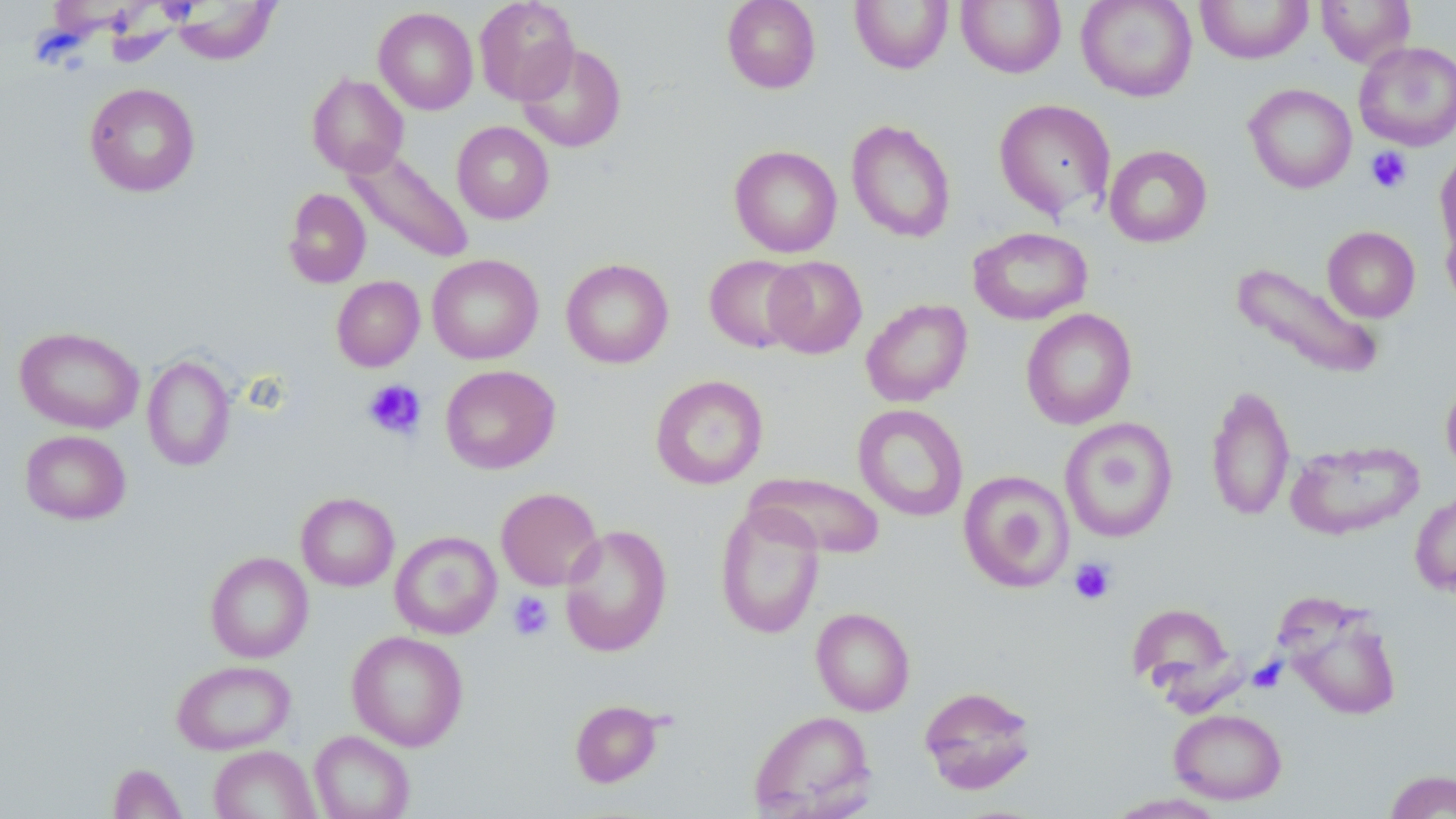

slide_level_diagnosis: no evidence of blood parasites
image_size: 1456×819 pixels
platelet_locations: 'approximate bounding boxes as [x1, y1, x2, y2] in pixels: [1365, 146, 1412, 194], [362, 379, 427, 440], [1069, 558, 1116, 605], [508, 591, 554, 640]'
modality: light microscopy
uninfected_red_blood_cell_locations: 'approximate bounding boxes as [x1, y1, x2, y2] in pixels: [473, 0, 579, 104], [721, 0, 821, 93], [850, 0, 952, 74], [956, 0, 1066, 78], [1076, 0, 1198, 102], [1195, 0, 1313, 64], [1316, 0, 1416, 68], [172, 1, 280, 65], [374, 7, 478, 114], [1353, 41, 1456, 151], [517, 43, 626, 152], [306, 73, 409, 178], [84, 82, 200, 197], [1244, 84, 1357, 193], [993, 98, 1115, 221], [846, 119, 956, 243], [452, 121, 554, 224], [1103, 144, 1213, 248], [729, 145, 843, 258], [1436, 146, 1456, 264], [345, 148, 474, 265], [283, 187, 371, 288], [1440, 208, 1456, 314], [1322, 226, 1420, 322], [968, 227, 1092, 325], [427, 254, 543, 364], [704, 255, 808, 353], [763, 255, 867, 359], [561, 258, 674, 369], [1232, 262, 1385, 380], [331, 276, 425, 372], [861, 298, 973, 407], [1021, 308, 1137, 430], [15, 326, 144, 434], [142, 355, 235, 471], [440, 365, 561, 474], [1440, 373, 1456, 478], [650, 374, 767, 489], [1205, 384, 1295, 522], [853, 404, 968, 522], [1060, 418, 1177, 543], [20, 430, 131, 525], [1285, 439, 1424, 540], [746, 470, 885, 560], [958, 470, 1074, 593], [496, 487, 603, 591], [1410, 490, 1456, 598], [296, 492, 399, 591], [715, 503, 825, 639], [559, 523, 673, 657], [390, 531, 502, 639], [205, 551, 313, 663], [1279, 597, 1403, 721], [1127, 600, 1236, 700], [811, 607, 915, 715], [347, 630, 468, 751], [172, 659, 295, 754], [919, 685, 1038, 795], [570, 699, 664, 788], [1169, 708, 1287, 804], [749, 710, 876, 818], [309, 731, 415, 819], [208, 745, 320, 819], [108, 763, 188, 819], [1384, 769, 1456, 819], [1105, 792, 1230, 818]'
field_of_view: one of a larger specimen
magnification: 1000x
preparation: thin blood smear
stain: May-Grünwald-Giemsa